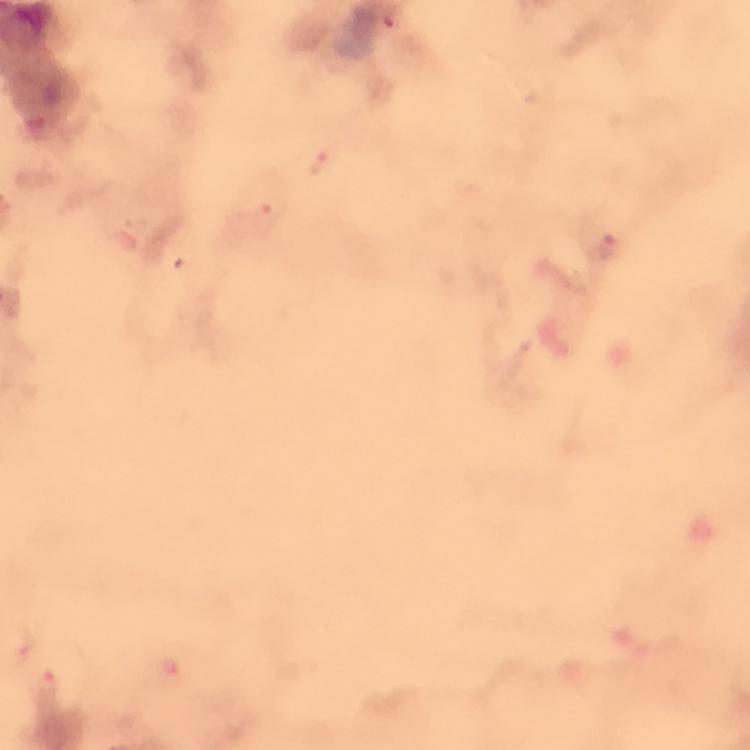 Approximate object centers, in pixels from the top-left corner. Malaria parasite locations: (x=319, y=163), (x=605, y=246), (x=46, y=684). Giemsa stain. A crop from one field of view. From a malaria diagnostic workup. Thick blood smear. At 100x magnification. Immersion oil was used. Photographed with a smartphone mounted on the microscope. Image is 750×750 pixels.